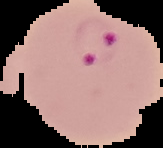 Segmented cell region on a black background. Image is 163×148 pixels. From a thin blood film. Malaria status: parasitized.